Describe the morphology of the erythrocytes.
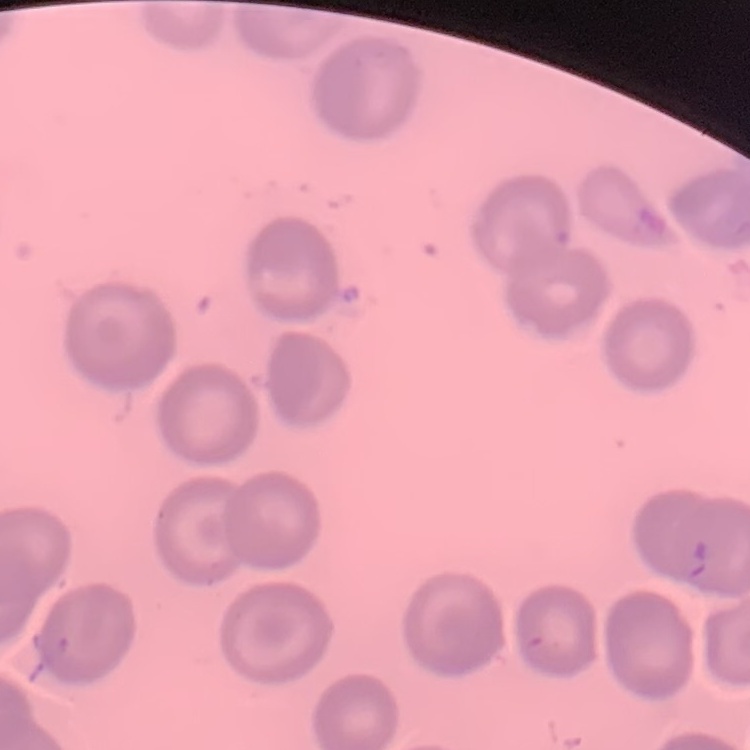

They show no rouleaux formation.

Square crop of a larger photomicrograph. Thin peripheral smear. Stained with either Field's or Giemsa.